Give the extent of all Plasmodium malariae-infected red blood cells.
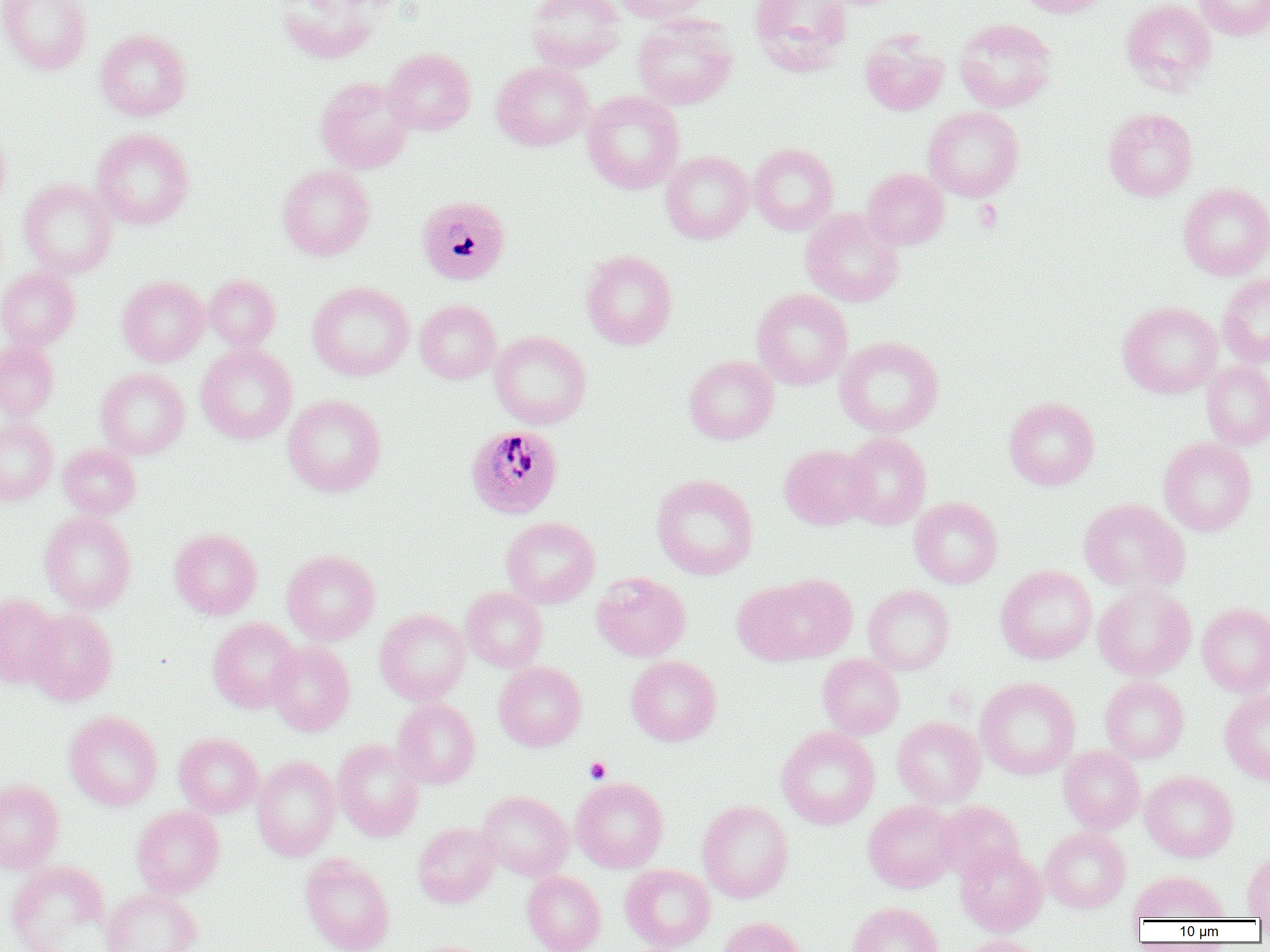
Approximate bounding boxes as (x1,y1)-(x2,y2) corner pairs in pixels.
Plasmodium malariae-infected red blood cells: (415,196)-(511,285), (465,424)-(564,519).

Summary:
  - Uninfected red blood cell locations: (0,0)-(92,75), (274,0)-(381,64), (525,0)-(626,73), (611,0)-(715,24), (749,0)-(853,76), (1014,0)-(1113,18), (1121,0)-(1217,94), (1194,0)-(1270,41), (632,14)-(738,110), (953,17)-(1057,113), (95,29)-(191,121), (860,33)-(949,116), (383,47)-(476,135), (491,60)-(594,151), (315,76)-(414,173), (582,90)-(684,194), (923,106)-(1024,202), (1103,107)-(1198,201), (0,123)-(11,215), (91,127)-(194,229), (748,143)-(838,235), (660,151)-(754,244), (277,164)-(375,260), (861,168)-(950,250), (19,179)-(117,277), (1178,183)-(1270,280), (801,208)-(904,307), (580,250)-(678,350), (0,267)-(81,350), (1217,272)-(1270,367), (117,275)-(209,366), (203,275)-(281,349), (307,281)-(414,381), (751,289)-(853,390), (415,299)-(501,384), (1118,301)-(1222,398), (489,331)-(591,429), (835,336)-(944,437), (0,340)-(59,421), (196,343)-(297,444), (684,355)-(779,444), (1201,361)-(1270,449), (96,368)-(190,458), (282,394)-(386,497), (1004,397)-(1100,490), (0,419)-(58,505), (841,432)-(932,530), (1159,437)-(1257,535), (58,444)-(140,519), (779,444)-(874,530), (652,473)-(758,580), (910,497)-(1003,589), (1079,499)-(1190,593), (40,512)-(137,613), (501,517)-(600,608), (169,529)-(262,619), (282,550)-(379,644), (995,565)-(1096,664), (990,569)-(1086,785), (592,572)-(691,661), (740,573)-(857,665), (1093,583)-(1196,681), (863,584)-(954,674), (460,587)-(547,671), (0,593)-(63,688), (1197,603)-(1270,697), (25,609)-(117,706), (374,609)-(470,705), (208,617)-(301,713), (266,641)-(355,736), (817,654)-(905,739), (626,655)-(722,746), (494,661)-(586,751), (1100,675)-(1189,763), (976,677)-(1080,780), (1219,689)-(1270,785), (392,698)-(481,789), (64,711)-(163,811), (892,716)-(986,808), (776,726)-(880,829), (174,733)-(264,818), (332,738)-(426,841), (1058,745)-(1145,833), (252,755)-(341,861), (1140,771)-(1238,862), (571,777)-(669,873), (0,780)-(63,873), (478,790)-(574,881), (697,800)-(794,903), (863,800)-(960,893), (934,801)-(1024,882), (131,805)-(225,897), (413,822)-(501,907), (1041,827)-(1131,913), (955,844)-(1048,937), (1241,852)-(1270,919), (300,853)-(395,952), (5,860)-(112,951), (620,864)-(716,951), (522,871)-(605,952), (1127,871)-(1229,922), (100,888)-(202,952), (848,902)-(945,952), (717,916)-(806,952), (956,935)-(1045,952)
  - Platelet locations: (974,200)-(1002,232), (585,757)-(611,783)
  - Slide-level diagnosis: Plasmodium malariae
  - Field of view: single
  - Magnification: 1000x
  - Image size: 1270×952 pixels
  - Modality: optical microscopy
  - Preparation: thin blood smear